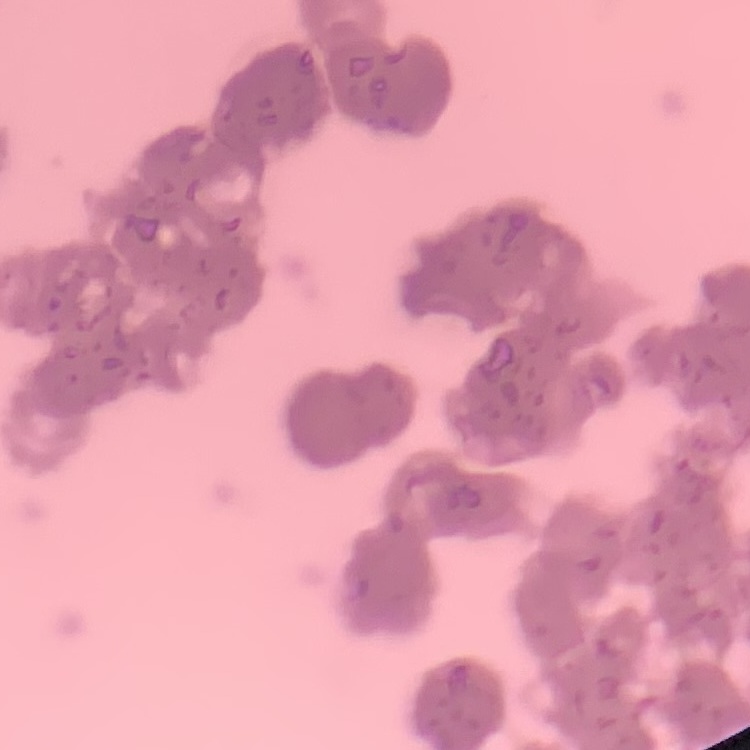

red blood cell morphology = rouleaux formation
preparation = thin blood film
stain = Field's or Giemsa
image type = one tile cut from a larger photomicrograph